Report the malaria status of this cell.
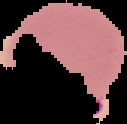
Parasitized.

preparation = thin blood film
image type = cell region segmented out of the field of view; surrounding area masked to black
image size = 127×124 pixels